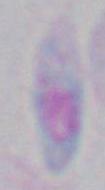 Toxoplasma gondii is shown. Micrograph. Captured at 1000x magnification.